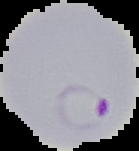

Summary:
  - Malaria status: parasitized
  - Image type: cell region segmented out of the field of view; surrounding area masked to black
  - Image size: 139×151 pixels
  - Preparation: thin blood smear